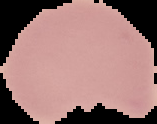
Image is 157×124 pixels. Result: no malaria parasites seen. Cell region segmented out of the field of view; the surrounding area is masked to black. From a thin blood film.